Name the cell type shown.
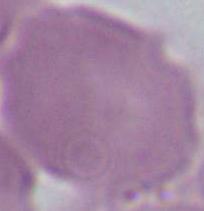
This is an erythrocyte.

{
  "magnification": "1000x",
  "modality": "photomicrograph"
}